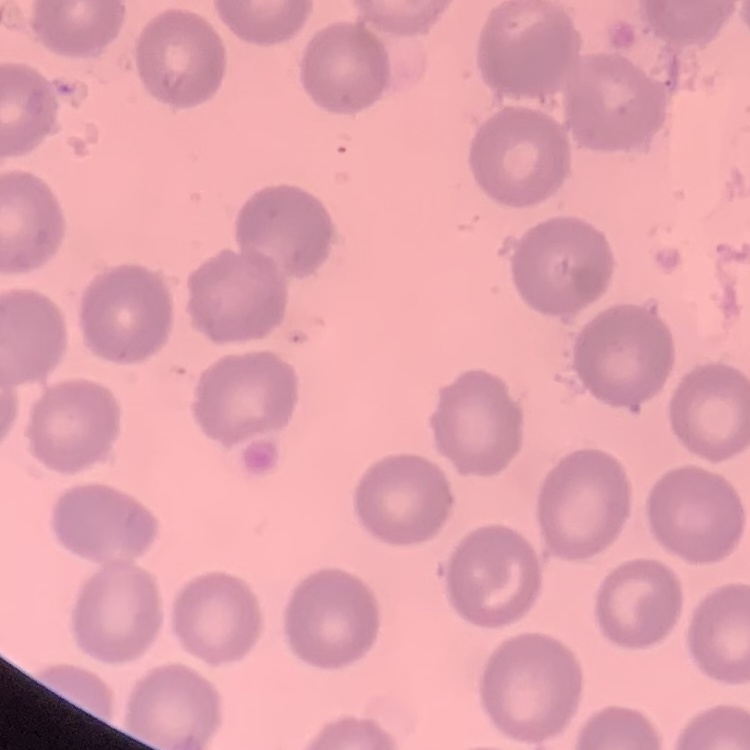
Summary:
  - Erythrocyte morphology: no rouleaux formation
  - Preparation: thin peripheral smear
  - Stain: Field's or Giemsa
  - Image type: one tile cut from a larger photomicrograph